Classify this cell by malaria status.
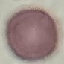

It is uninfected.

Giemsa stain. Photographed with a smartphone camera at the microscope eyepiece. Thin smear of blood. Automatically extracted cell patch, resized to 64 × 64 pixels.